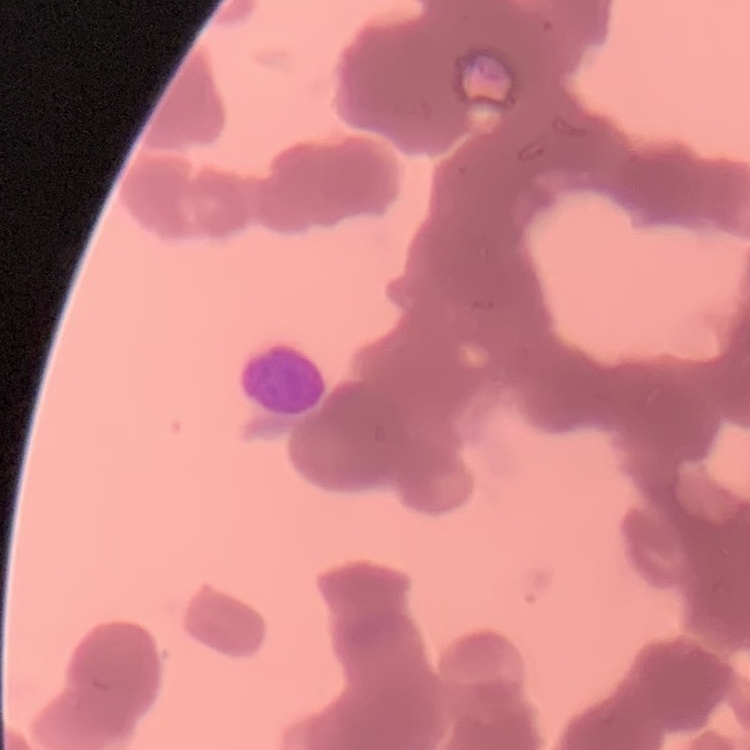

The erythrocytes exhibit rouleaux formation. Thin blood smear. Field's or Giemsa stain. Square crop of a larger photomicrograph.